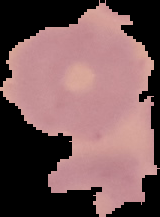
{
  "preparation": "thin blood film",
  "image_type": "segmented cell region on a black background",
  "image_size": "160×217 pixels",
  "malaria_status": "uninfected"
}